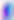
{
  "identification": "Toxoplasma gondii",
  "magnification": "400x",
  "modality": "micrograph"
}